Assess for malaria.
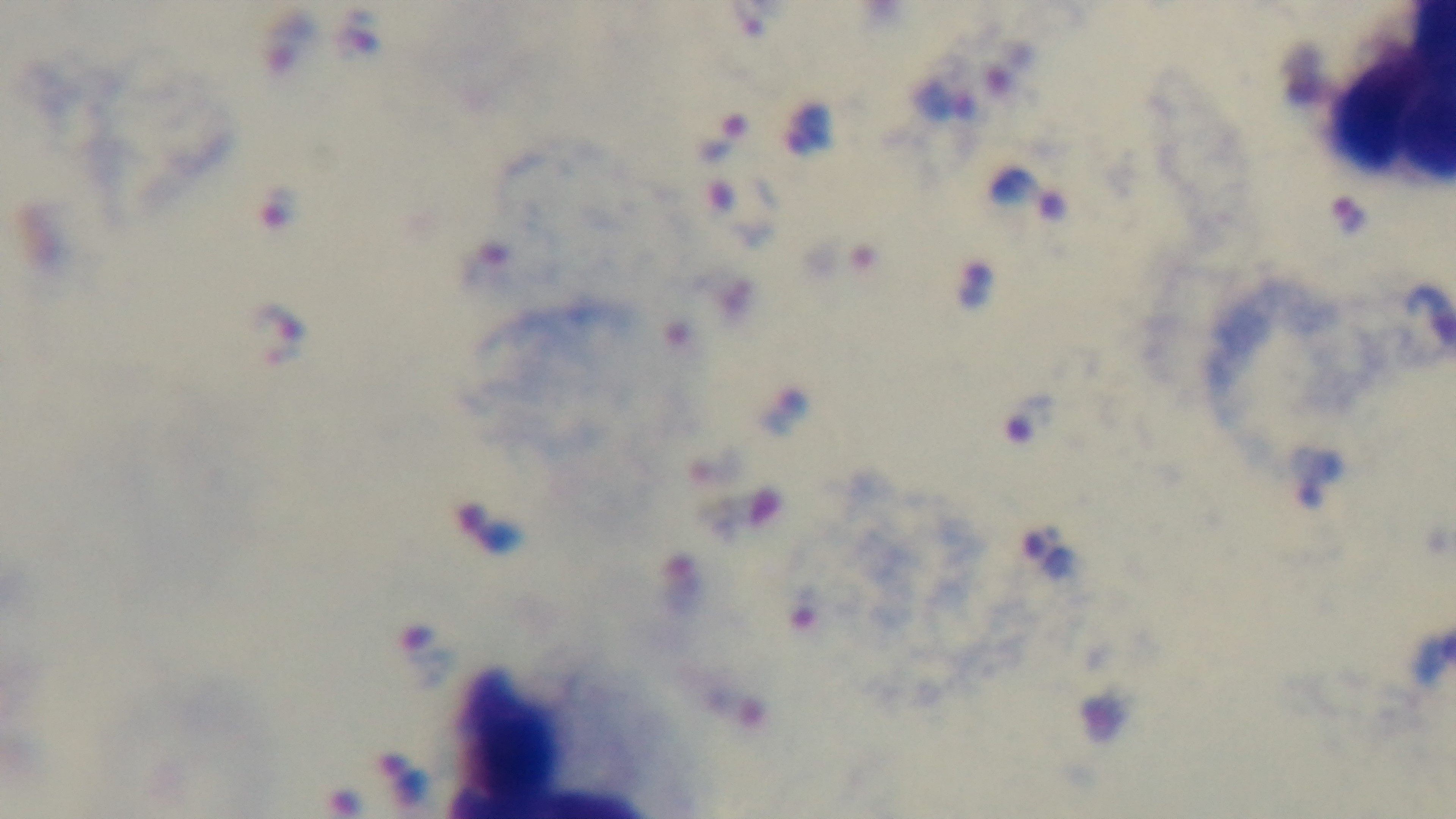

It is infected.

field of view = one from the slide
stain = Giemsa
capture = mounted 4K digital camera
modality = light microscopy
preparation = thick blood film
objective = 100x oil immersion